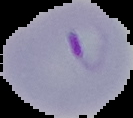
preparation = thin blood film
image size = 133×118 pixels
image type = cell region segmented out of the field of view; surrounding area masked to black
malaria status = parasitized